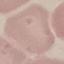

malaria status = uninfected
preparation = thin smear
capture = smartphone through the microscope eyepiece
image type = automatically extracted cell patch, resized to 64 × 64 pixels
stain = Giemsa